Identify the cell.
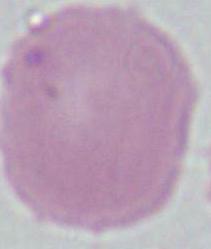
An erythrocyte.

magnification = 1000x
modality = photomicrograph